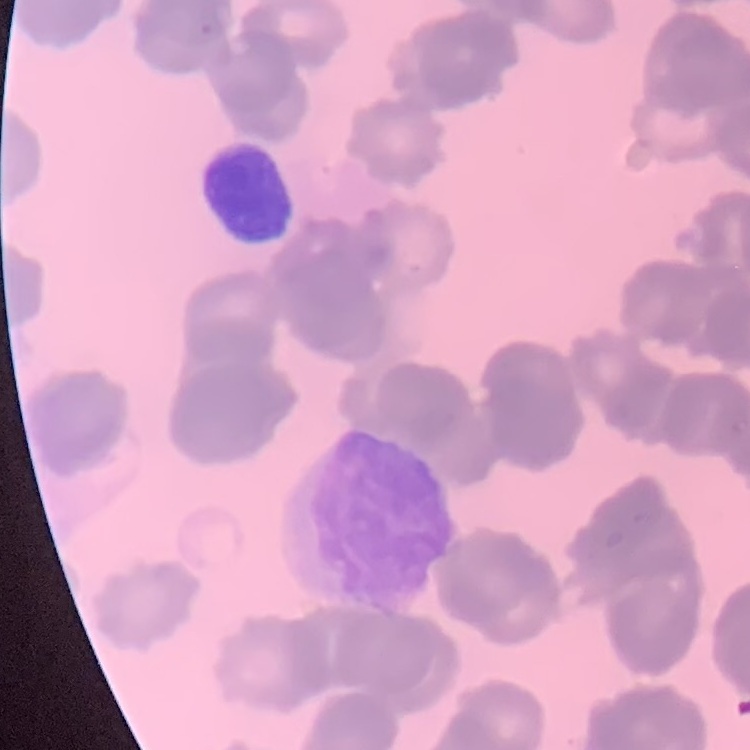
Summary:
  - Erythrocyte morphology: rouleaux formation
  - Stain: Field's or Giemsa
  - Preparation: thin blood smear
  - Image type: square crop of a larger photomicrograph